State the preparation type.
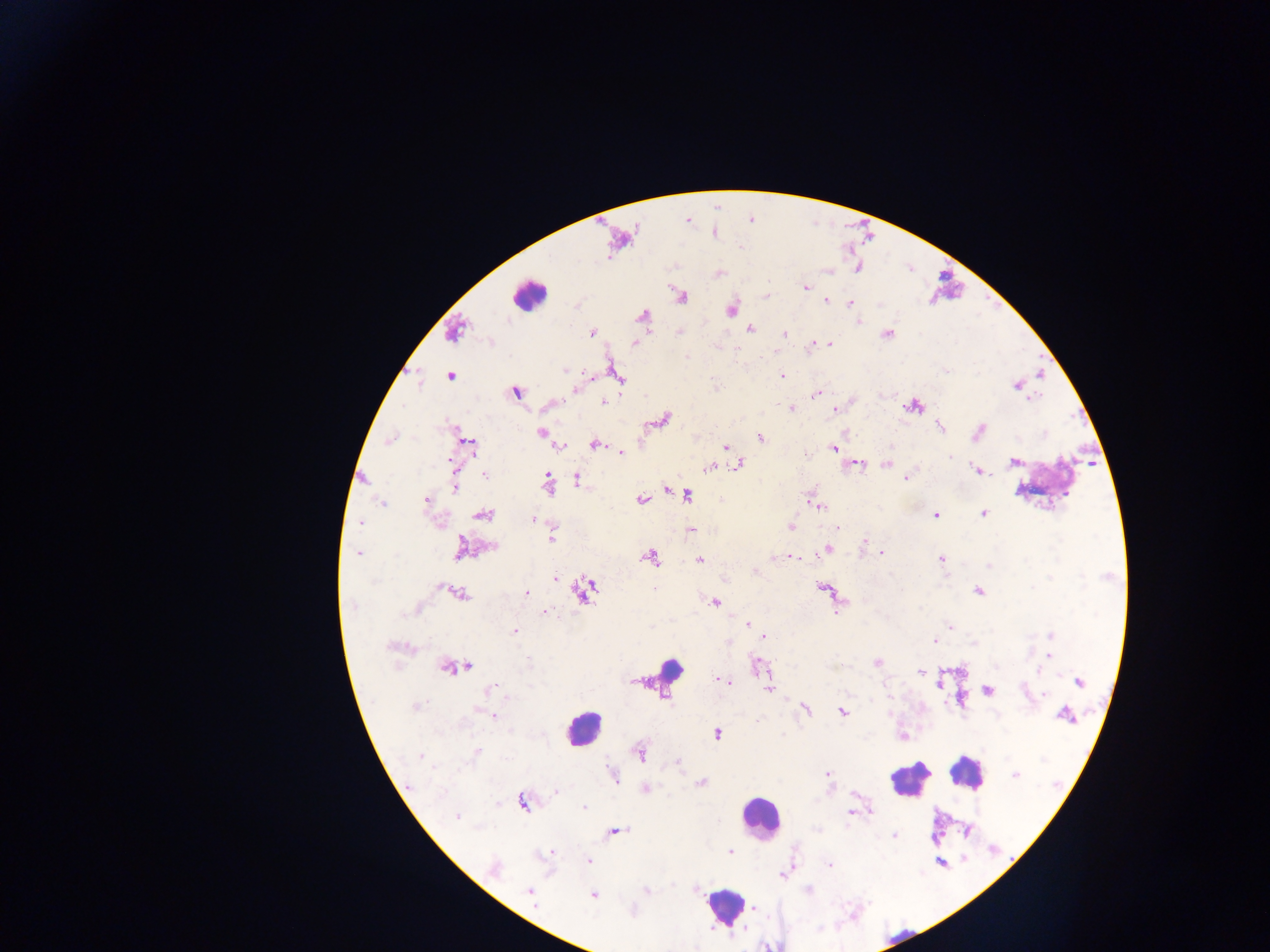

Thick blood film.

Approximate centers as x y in pixels. Plasmodium parasite locations: 805 288; 826 300; 850 303; 750 329; 591 333; 784 333; 828 343; 634 344; 812 346; 687 356; 565 370; 781 375; 450 376; 1017 385; 575 389; 516 392; 814 395; 1031 399; 604 403; 791 409; 836 410; 939 427; 979 430; 542 432; 760 437; 390 440; 470 444; 595 444; 561 446; 892 446; 726 448; 833 448; 621 452; 948 457; 451 462; 1013 462; 857 463; 738 464; 885 464; 708 468; 978 471; 485 476; 577 478; 547 479; 906 479; 455 488; 665 489; 687 495; 721 499; 427 500; 640 500; 382 504; 820 507; 484 514; 983 514; 936 515; 533 519; 360 523; 791 527; 838 528; 688 529; 553 539; 864 541; 493 546; 460 549; 826 549; 881 553; 358 554; 793 557; 651 558; 941 559; 699 560; 988 565; 755 572; 556 579; 586 589; 654 589; 979 591; 460 594; 526 594; 716 603; 353 606; 546 611; 748 624; 951 627; 515 632; 1050 635; 765 637; 935 640; 974 644; 1048 656; 528 661; 877 662; 464 666; 448 667; 1037 671; 919 672; 724 681; 940 682; 1080 682; 768 687; 490 689; 988 691; 1044 695; 416 706; 806 710; 842 712; 493 716; 1066 716; 757 720; 717 734; 640 753; 475 754; 421 756; 677 761; 1015 774; 827 775; 614 776; 701 783; 409 785; 646 788; 556 791; 523 803; 584 807; 871 811; 851 812; 457 816; 616 831; 894 836; 730 851; 550 852; 589 861; 829 866; 495 867; 782 874; 646 890; 808 890; 529 891; 592 895; 753 908. Leukocyte locations: 528 295; 668 668; 583 727; 965 773; 909 780; 759 816; 723 907. Sample from Ghana. Image is 1270×952 pixels. Single field of view. Mobile-phone photograph taken through the microscope.